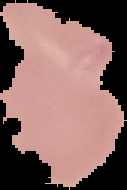 From a thin blood smear. Cell region segmented out of the field of view; the surrounding area is masked to black. Image is 127×190 pixels. Malaria status: uninfected.